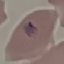

malaria status = parasitized
image type = cell patch, automatically extracted from a larger field of view and resized to 64 × 64 pixels
capture = smartphone through the microscope eyepiece
preparation = thin blood smear
stain = Giemsa